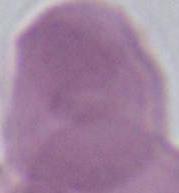
Summary:
  - Identification: erythrocyte
  - Modality: micrograph
  - Magnification: 1000x